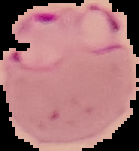 Malaria status: parasitized. From a thin blood film. The area outside the segmented cell region is set to black. Image is 139×151 pixels.